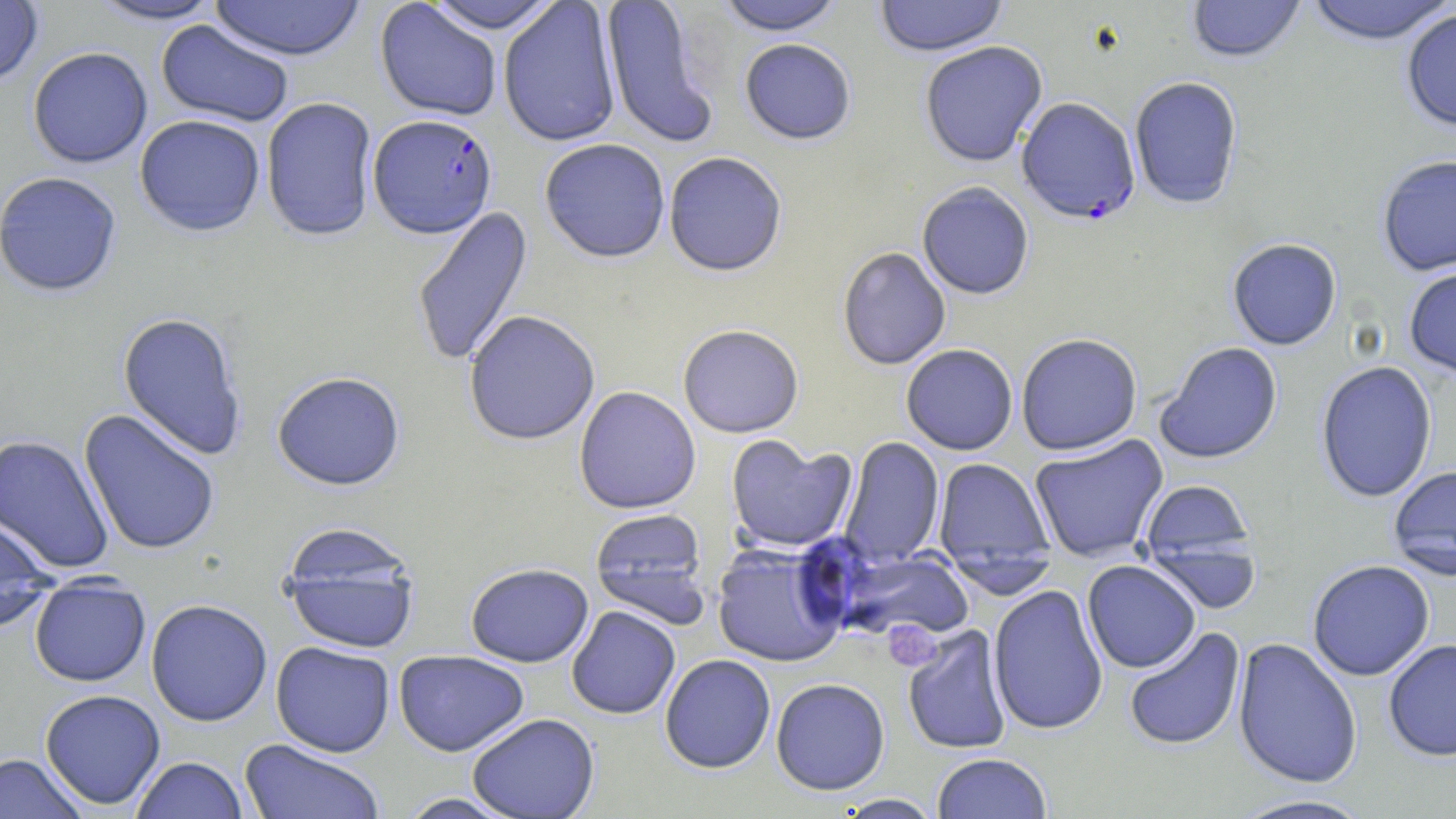

slide-level diagnosis = Plasmodium falciparum
field of view = single
image size = 1456×819 pixels
Plasmodium falciparum-infected red blood cell locations = approximate bounding boxes as named x1/y1/x2/y2 corners in pixels: (x1=1016, y1=98, x2=1141, y2=226), (x1=368, y1=114, x2=497, y2=240)
platelet locations = approximate bounding boxes as named x1/y1/x2/y2 corners in pixels: (x1=880, y1=620, x2=946, y2=671)
magnification = 1000x
modality = light microscopy
preparation = thin blood smear
uninfected red blood cell locations = approximate bounding boxes as named x1/y1/x2/y2 corners in pixels: (x1=0, y1=0, x2=44, y2=88), (x1=87, y1=0, x2=225, y2=26), (x1=208, y1=0, x2=366, y2=62), (x1=422, y1=0, x2=564, y2=35), (x1=600, y1=0, x2=719, y2=150), (x1=715, y1=0, x2=846, y2=37), (x1=874, y1=0, x2=1008, y2=59), (x1=1186, y1=0, x2=1306, y2=65), (x1=1303, y1=0, x2=1455, y2=47), (x1=374, y1=1, x2=502, y2=122), (x1=498, y1=1, x2=622, y2=148), (x1=1401, y1=9, x2=1456, y2=134), (x1=155, y1=19, x2=294, y2=128), (x1=739, y1=39, x2=857, y2=147), (x1=920, y1=42, x2=1048, y2=168), (x1=27, y1=47, x2=153, y2=168), (x1=1130, y1=77, x2=1243, y2=210), (x1=261, y1=97, x2=378, y2=243), (x1=134, y1=114, x2=266, y2=237), (x1=539, y1=140, x2=671, y2=265), (x1=664, y1=153, x2=788, y2=280), (x1=1376, y1=155, x2=1456, y2=277), (x1=0, y1=171, x2=123, y2=297), (x1=917, y1=183, x2=1034, y2=301), (x1=411, y1=205, x2=534, y2=369), (x1=1227, y1=239, x2=1342, y2=351), (x1=837, y1=247, x2=951, y2=371), (x1=1403, y1=264, x2=1456, y2=380), (x1=117, y1=311, x2=247, y2=461), (x1=463, y1=311, x2=601, y2=447), (x1=678, y1=326, x2=803, y2=439), (x1=1016, y1=334, x2=1143, y2=456), (x1=1155, y1=342, x2=1283, y2=465), (x1=901, y1=345, x2=1018, y2=455), (x1=1316, y1=361, x2=1438, y2=503), (x1=271, y1=372, x2=406, y2=491), (x1=574, y1=386, x2=701, y2=515), (x1=79, y1=409, x2=221, y2=556), (x1=0, y1=434, x2=115, y2=574), (x1=1029, y1=434, x2=1169, y2=562), (x1=725, y1=436, x2=856, y2=554), (x1=839, y1=437, x2=945, y2=566), (x1=932, y1=458, x2=1055, y2=578), (x1=1388, y1=466, x2=1456, y2=580), (x1=1138, y1=480, x2=1257, y2=594), (x1=589, y1=509, x2=712, y2=629), (x1=0, y1=514, x2=59, y2=633), (x1=278, y1=524, x2=421, y2=655), (x1=712, y1=542, x2=848, y2=668), (x1=832, y1=548, x2=975, y2=643), (x1=1082, y1=560, x2=1201, y2=673), (x1=1307, y1=560, x2=1435, y2=681), (x1=465, y1=563, x2=594, y2=667), (x1=30, y1=579, x2=151, y2=687), (x1=987, y1=584, x2=1109, y2=736), (x1=145, y1=599, x2=273, y2=727), (x1=566, y1=606, x2=681, y2=720), (x1=902, y1=625, x2=1012, y2=755), (x1=1123, y1=626, x2=1246, y2=752), (x1=1232, y1=637, x2=1363, y2=788), (x1=1382, y1=639, x2=1456, y2=761), (x1=270, y1=641, x2=395, y2=757), (x1=394, y1=650, x2=530, y2=756), (x1=660, y1=654, x2=776, y2=773), (x1=660, y1=668, x2=890, y2=780), (x1=770, y1=678, x2=890, y2=795), (x1=39, y1=689, x2=166, y2=809), (x1=467, y1=713, x2=600, y2=818), (x1=239, y1=739, x2=385, y2=819), (x1=0, y1=752, x2=89, y2=819), (x1=932, y1=753, x2=1052, y2=819), (x1=130, y1=756, x2=249, y2=818), (x1=395, y1=792, x2=521, y2=818), (x1=833, y1=793, x2=943, y2=818), (x1=1228, y1=794, x2=1377, y2=818)
stain = May-Grünwald-Giemsa